Assess this cell for malaria.
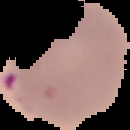
Parasitized.

Image is 130×130 pixels. From a thin blood film. The area outside the segmented cell region is set to black.